Assess the morphology of the red blood cells.
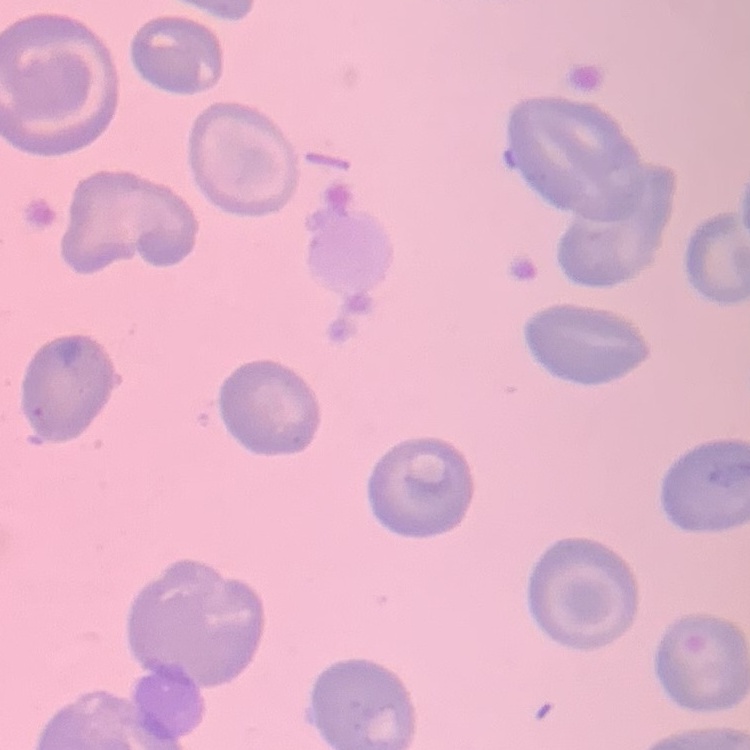
No rouleaux formation.

{
  "preparation": "thin blood smear",
  "stain": "Field's or Giemsa",
  "image_type": "one tile cut from a larger photomicrograph"
}